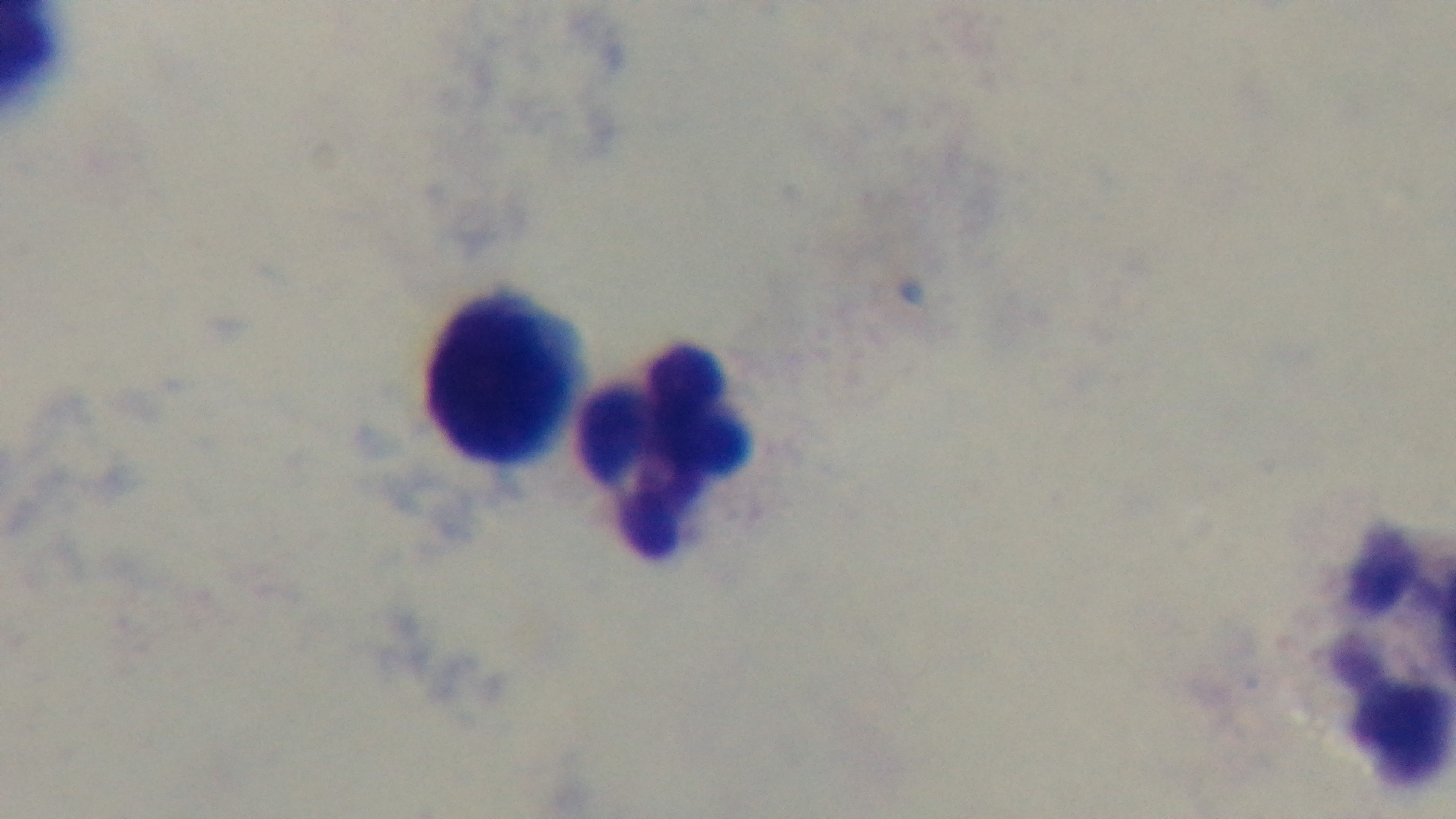

{
  "objective": "100x oil immersion",
  "malaria_status": "negative",
  "field_of_view": "single",
  "capture": "mounted 4K digital camera",
  "modality": "light microscopy",
  "stain": "Giemsa",
  "preparation": "thick blood film"
}